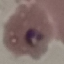

result = malaria parasites detected
preparation = thin blood smear
stain = Giemsa
capture = smartphone through the microscope eyepiece
image type = automatically extracted cell patch, resized to 64 × 64 pixels